Describe the morphology of the erythrocytes.
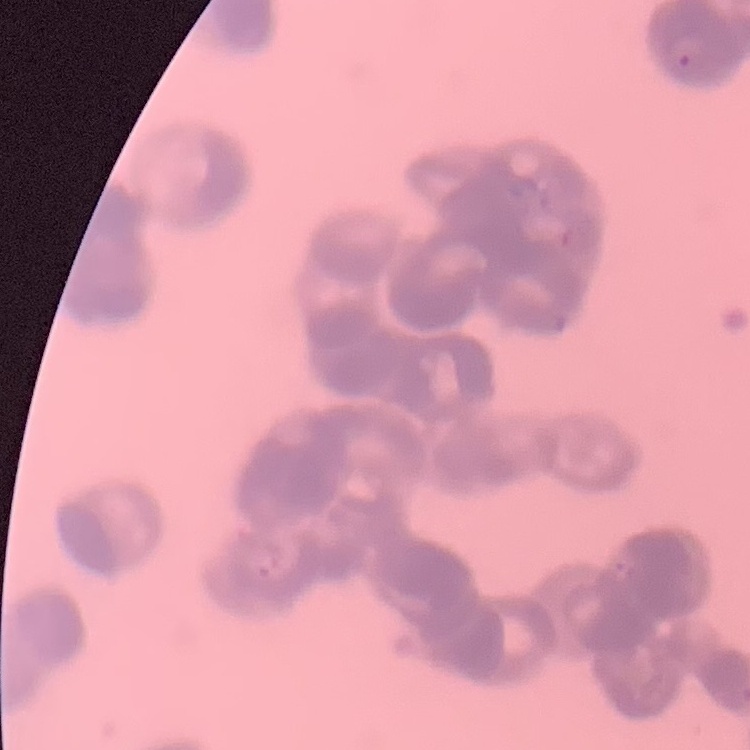
Rouleaux formation.

Square crop of a larger photomicrograph. Stained with either Field's or Giemsa. Thin blood film.